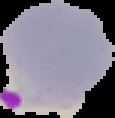
Summary:
  - Image type: segmented cell region with the area outside set to black
  - Preparation: thin blood smear
  - Image size: 115×118 pixels
  - Result: Plasmodium parasites identified